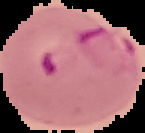

Image is 145×133 pixels. Result: malaria parasites detected. The area outside the segmented cell region is set to black. From a thin blood film.